Locate every blood parasite and identify its species.
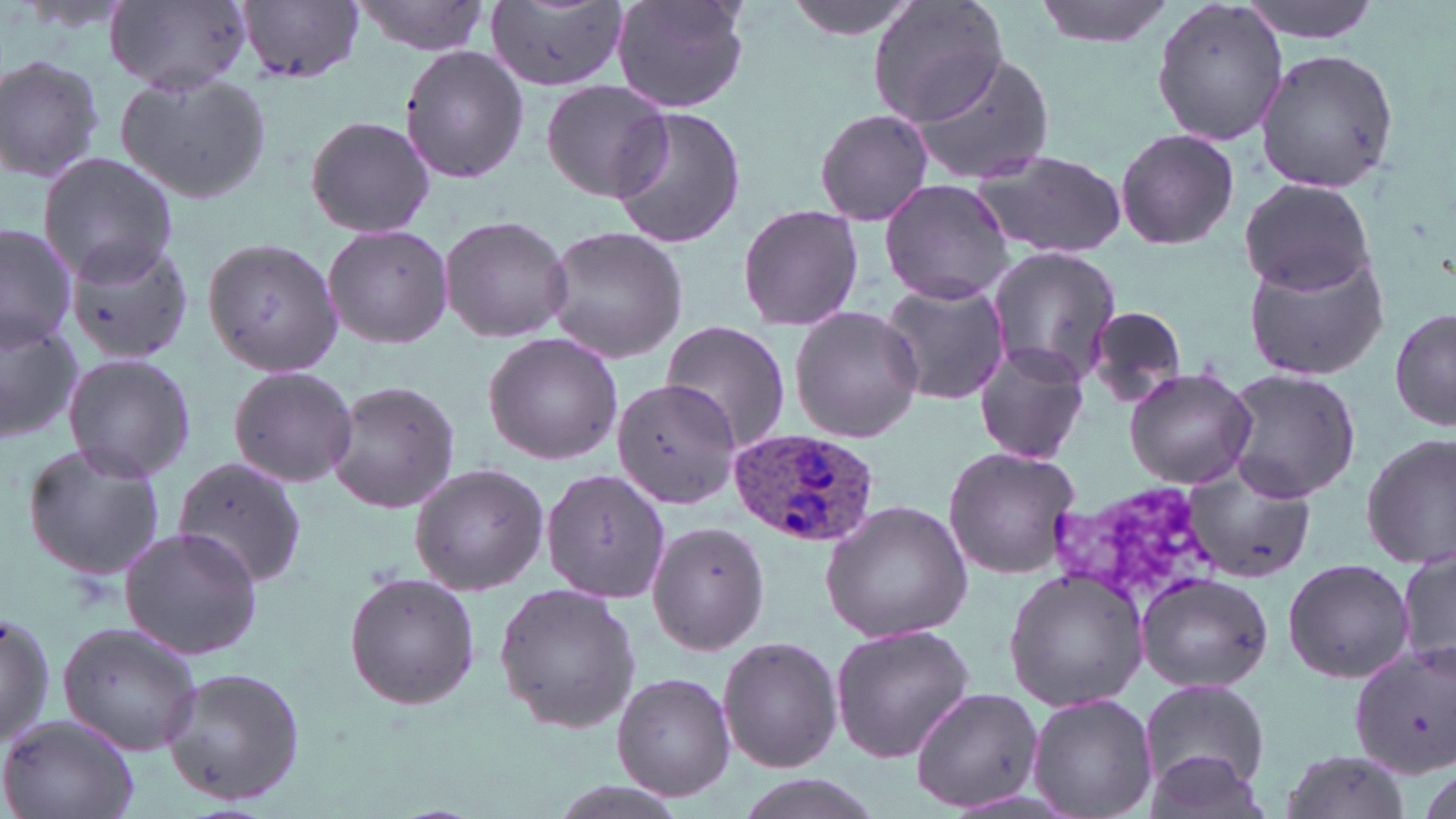

Approximate bounding boxes as [x1, y1, x2, y2] in pixels.
Plasmodium ovale-infected red blood cells: [727, 430, 882, 549].
No Plasmodium falciparum, Plasmodium malariae, Plasmodium vivax, Babesia divergens, or Trypanosoma brucei observed.

Summary:
  - Uninfected red blood cell locations: [104, 0, 253, 94], [238, 0, 366, 84], [350, 0, 491, 56], [610, 0, 752, 113], [786, 0, 923, 40], [868, 0, 1008, 129], [1034, 0, 1177, 46], [1234, 0, 1388, 41], [488, 1, 628, 94], [1153, 2, 1287, 148], [398, 43, 532, 185], [904, 48, 1058, 188], [1254, 52, 1399, 191], [0, 54, 106, 184], [116, 69, 274, 205], [539, 78, 671, 202], [610, 104, 747, 250], [811, 106, 935, 226], [305, 113, 438, 239], [1114, 128, 1239, 250], [968, 148, 1129, 259], [38, 153, 181, 283], [879, 178, 1016, 306], [1239, 178, 1379, 294], [737, 205, 863, 332], [440, 212, 571, 344], [0, 223, 78, 352], [321, 223, 454, 351], [541, 226, 689, 364], [199, 233, 344, 380], [65, 235, 196, 366], [1241, 244, 1392, 382], [985, 245, 1122, 387], [878, 280, 1010, 407], [790, 306, 924, 442], [1082, 306, 1189, 411], [1390, 307, 1455, 432], [0, 311, 84, 444], [659, 321, 793, 455], [483, 332, 625, 466], [972, 340, 1093, 465], [61, 352, 197, 482], [227, 365, 359, 489], [1123, 368, 1259, 490], [1220, 368, 1362, 503], [610, 378, 739, 507], [326, 380, 461, 515], [1360, 432, 1456, 572], [18, 440, 169, 583], [941, 445, 1083, 581], [172, 457, 308, 589], [409, 463, 551, 595], [541, 468, 670, 604], [1179, 469, 1318, 583], [818, 499, 973, 643], [648, 521, 770, 654], [118, 525, 263, 660], [1395, 540, 1454, 679], [1283, 557, 1413, 684], [1003, 568, 1147, 713], [342, 571, 480, 710], [1135, 572, 1275, 692], [492, 583, 642, 734], [0, 610, 55, 750], [58, 621, 205, 756], [829, 622, 977, 765], [718, 637, 843, 773], [1349, 646, 1455, 778], [159, 666, 309, 808], [612, 672, 736, 800], [1138, 678, 1269, 799], [912, 687, 1045, 812], [1027, 693, 1158, 819], [0, 714, 142, 819], [1137, 748, 1276, 819], [1278, 748, 1413, 819], [726, 772, 890, 819]
  - Slide-level diagnosis: Plasmodium ovale
  - Preparation: thin blood smear
  - Magnification: 1000x
  - Modality: optical microscopy
  - Image size: 1456×819 pixels
  - Stain: May-Grünwald-Giemsa
  - Field of view: one of a larger specimen